Identify the blood parasite species.
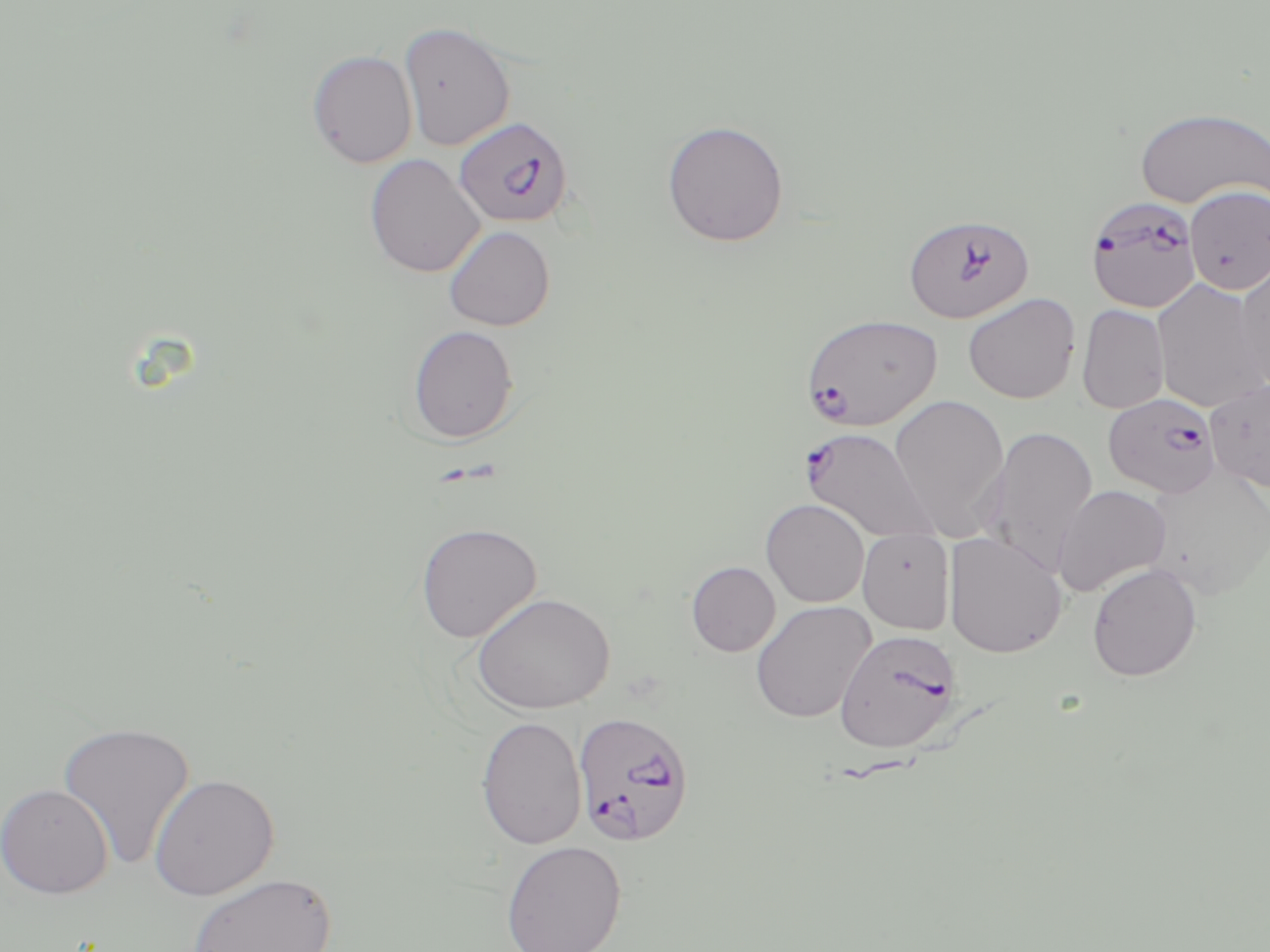

Plasmodium falciparum.

Summary:
  - Coordinate format: approximate bounding boxes as named x1/y1/x2/y2 corners in pixels
  - Plasmodium falciparum-infected red blood cell locations: (x1=454, y1=115, x2=574, y2=228), (x1=1085, y1=196, x2=1203, y2=313), (x1=903, y1=212, x2=1035, y2=323), (x1=801, y1=313, x2=943, y2=430), (x1=1103, y1=392, x2=1221, y2=498), (x1=800, y1=426, x2=939, y2=545), (x1=835, y1=628, x2=963, y2=753), (x1=573, y1=710, x2=697, y2=847)
  - Uninfected red blood cell locations: (x1=399, y1=21, x2=516, y2=151), (x1=306, y1=49, x2=418, y2=168), (x1=1134, y1=106, x2=1269, y2=210), (x1=661, y1=120, x2=789, y2=247), (x1=364, y1=153, x2=485, y2=278), (x1=1185, y1=185, x2=1270, y2=295), (x1=443, y1=225, x2=555, y2=331), (x1=1234, y1=259, x2=1270, y2=392), (x1=1151, y1=278, x2=1268, y2=413), (x1=963, y1=293, x2=1080, y2=404), (x1=1076, y1=304, x2=1170, y2=414), (x1=407, y1=325, x2=519, y2=444), (x1=1204, y1=379, x2=1270, y2=493), (x1=888, y1=394, x2=1011, y2=540), (x1=983, y1=425, x2=1098, y2=575), (x1=1052, y1=484, x2=1172, y2=597), (x1=760, y1=498, x2=869, y2=608), (x1=415, y1=522, x2=542, y2=642), (x1=858, y1=528, x2=956, y2=634), (x1=943, y1=531, x2=1067, y2=658), (x1=686, y1=561, x2=780, y2=656), (x1=1086, y1=563, x2=1202, y2=681), (x1=471, y1=592, x2=616, y2=715), (x1=750, y1=601, x2=876, y2=723), (x1=475, y1=715, x2=587, y2=850), (x1=56, y1=720, x2=195, y2=870), (x1=148, y1=772, x2=280, y2=901), (x1=0, y1=782, x2=113, y2=899), (x1=501, y1=840, x2=627, y2=951), (x1=187, y1=871, x2=337, y2=951)
  - Magnification: 1000x
  - Image size: 1270×952 pixels
  - Stain: May-Grünwald-Giemsa
  - Field of view: single
  - Modality: optical microscopy
  - Preparation: thin blood smear